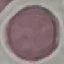

result = no malaria parasites seen
image type = automatically extracted cell patch, resized to 64 × 64 pixels
preparation = thin smear
stain = Giemsa
capture = smartphone camera at the microscope eyepiece